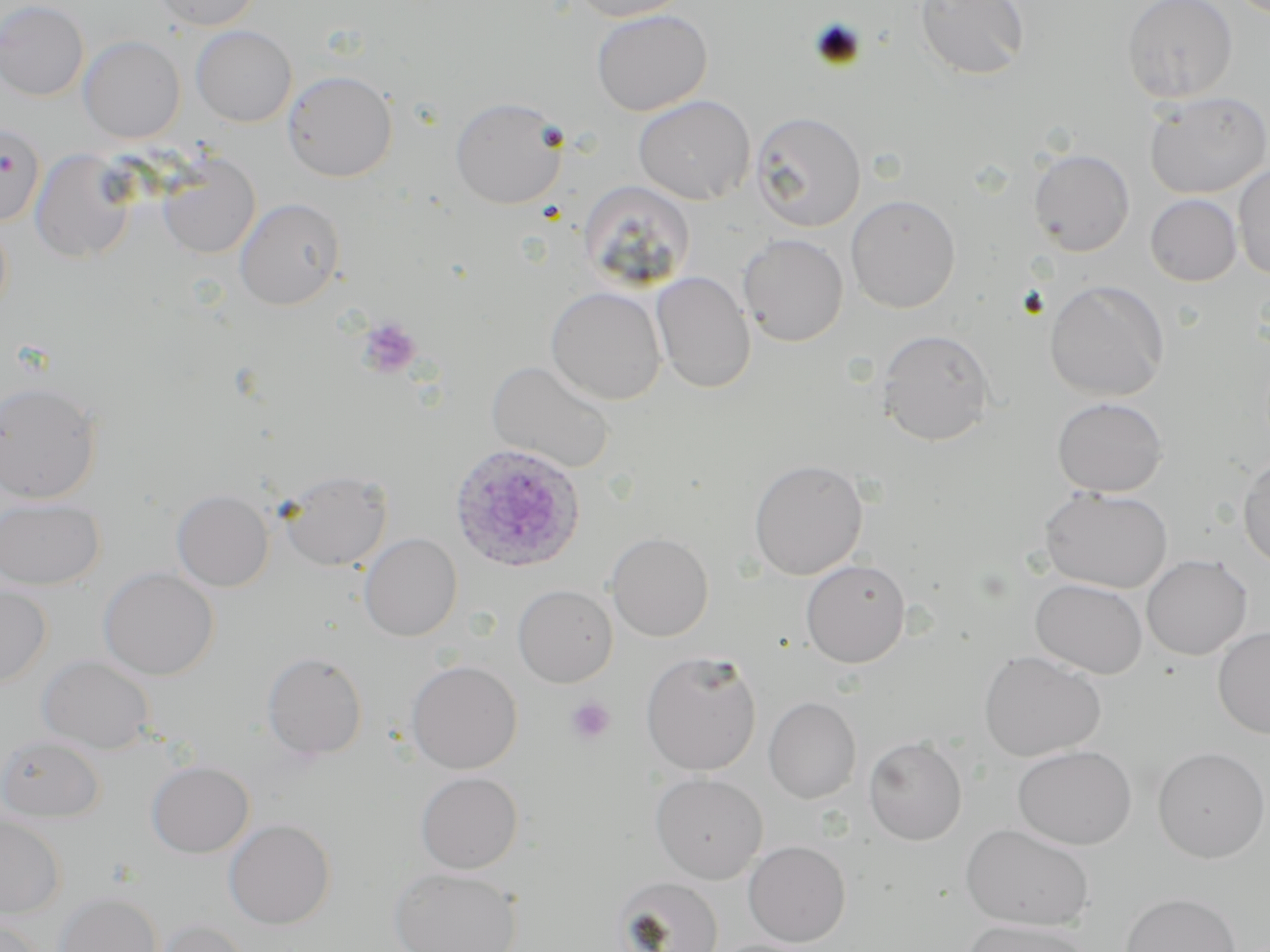
Approximate bounding boxes as (x1,y1)-(x2,y2) corner pairs in pixels. Plasmodium ovale-infected red blood cell locations: (449,442)-(586,573). Platelet locations: (806,16)-(867,69), (356,317)-(422,379), (566,697)-(615,745). Uninfected red blood cell locations: (0,0)-(90,101), (151,0)-(263,31), (567,0)-(691,21), (913,0)-(1030,81), (1121,0)-(1238,104), (591,9)-(713,116), (191,25)-(296,127), (78,35)-(185,144), (282,69)-(398,182), (1144,92)-(1270,199), (633,95)-(756,204), (450,96)-(568,209), (750,111)-(867,232), (0,122)-(45,226), (30,148)-(137,264), (1028,148)-(1135,256), (158,153)-(260,259), (1233,164)-(1270,280), (578,180)-(696,292), (846,194)-(961,313), (1145,194)-(1241,287), (234,197)-(345,310), (738,233)-(849,346), (651,270)-(756,394), (1044,279)-(1170,401), (545,286)-(667,405), (876,328)-(995,445), (486,360)-(616,474), (0,380)-(102,503), (1051,396)-(1168,497), (1237,455)-(1270,569), (748,459)-(868,580), (278,469)-(393,570), (1039,486)-(1173,593), (172,490)-(274,592), (0,497)-(105,591), (606,532)-(714,642), (359,533)-(462,641), (1141,554)-(1253,660), (801,558)-(910,668), (98,567)-(219,680), (1030,578)-(1148,678), (0,583)-(52,689), (513,584)-(618,687), (1213,625)-(1270,738), (640,650)-(762,776), (978,650)-(1106,762), (262,651)-(367,760), (37,654)-(155,753), (406,660)-(522,774), (763,696)-(862,804), (0,734)-(105,822), (863,737)-(967,845), (1012,745)-(1137,849), (1152,746)-(1270,863), (147,761)-(254,858), (415,771)-(523,874), (650,773)-(768,884), (0,816)-(67,919), (224,819)-(336,930), (961,823)-(1095,932), (743,840)-(851,946), (389,866)-(523,952), (612,876)-(724,952), (54,891)-(164,952), (1120,892)-(1241,952), (0,916)-(47,952), (147,917)-(251,952), (960,918)-(1093,952). Slide-level diagnosis: Plasmodium ovale. Thin blood film. One field of a larger specimen. Captured at 1000x magnification. Light microscopy. Image is 1270×952 pixels. May-Grünwald-Giemsa stain.